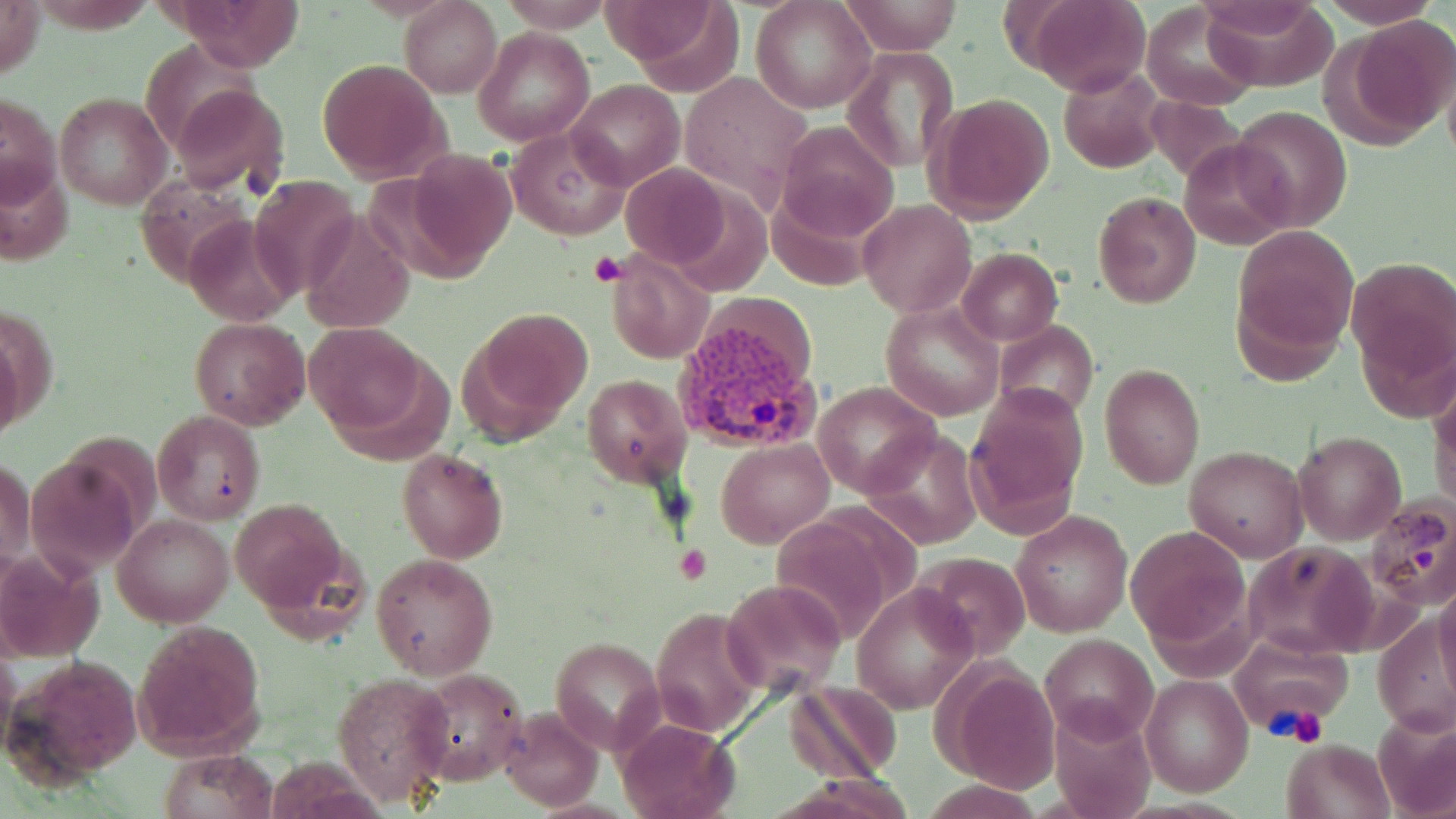
Summary:
  - Coordinate format: approximate bounding boxes as [x1, y1, x2, y2] in pixels
  - Plasmodium vivax-infected red blood cell locations: [674, 319, 826, 457], [1366, 495, 1455, 609]
  - Platelet locations: [589, 252, 626, 288], [677, 546, 711, 584], [1266, 704, 1327, 745]
  - Uninfected red blood cell locations: [0, 0, 46, 81], [173, 0, 304, 69], [752, 0, 876, 113], [841, 0, 965, 55], [1029, 0, 1151, 98], [1321, 0, 1440, 29], [401, 1, 501, 98], [608, 1, 743, 92], [1198, 1, 1333, 84], [1142, 4, 1258, 111], [1343, 14, 1456, 140], [474, 28, 593, 146], [842, 45, 958, 172], [317, 59, 449, 185], [1058, 67, 1165, 174], [566, 79, 684, 191], [167, 80, 290, 196], [2, 91, 61, 210], [54, 92, 172, 210], [927, 93, 1056, 223], [1231, 104, 1351, 231], [776, 120, 898, 241], [507, 128, 628, 239], [1181, 138, 1296, 250], [397, 150, 516, 275], [622, 163, 732, 268], [248, 177, 363, 300], [1093, 190, 1202, 309], [859, 201, 977, 318], [187, 213, 294, 326], [299, 213, 414, 333], [1234, 225, 1357, 362], [955, 248, 1061, 346], [604, 249, 716, 365], [1346, 256, 1455, 383], [880, 302, 1004, 421], [462, 307, 594, 440], [189, 317, 312, 430], [304, 322, 429, 436], [994, 322, 1099, 421], [1099, 362, 1205, 490], [1429, 368, 1456, 514], [583, 373, 691, 485], [814, 382, 940, 499], [965, 385, 1088, 532], [152, 410, 266, 524], [863, 427, 984, 549], [1293, 429, 1406, 544], [716, 438, 832, 548], [1184, 445, 1309, 562], [396, 448, 507, 564], [1, 456, 36, 570], [228, 497, 353, 621], [1011, 510, 1133, 637], [114, 511, 233, 626], [1126, 525, 1249, 648], [1241, 542, 1377, 657], [1, 546, 103, 662], [914, 551, 1032, 662], [370, 553, 498, 680], [721, 577, 848, 699], [1435, 581, 1456, 700], [853, 582, 977, 714], [648, 607, 764, 739], [1372, 615, 1455, 737], [134, 620, 265, 759], [1230, 632, 1353, 734], [1040, 634, 1158, 743], [550, 636, 664, 750], [12, 655, 146, 784], [938, 663, 1063, 791], [411, 667, 531, 786], [333, 672, 455, 808], [1139, 675, 1253, 797], [782, 682, 903, 783], [1048, 703, 1156, 819], [498, 706, 603, 811], [1373, 712, 1456, 818], [615, 718, 738, 819], [1279, 738, 1392, 819], [153, 750, 276, 819]
  - Slide-level diagnosis: Plasmodium vivax
  - Magnification: 1000x
  - Modality: optical microscopy
  - Image size: 1456×819 pixels
  - Preparation: thin blood film
  - Stain: May-Grünwald-Giemsa
  - Field of view: one of a larger specimen